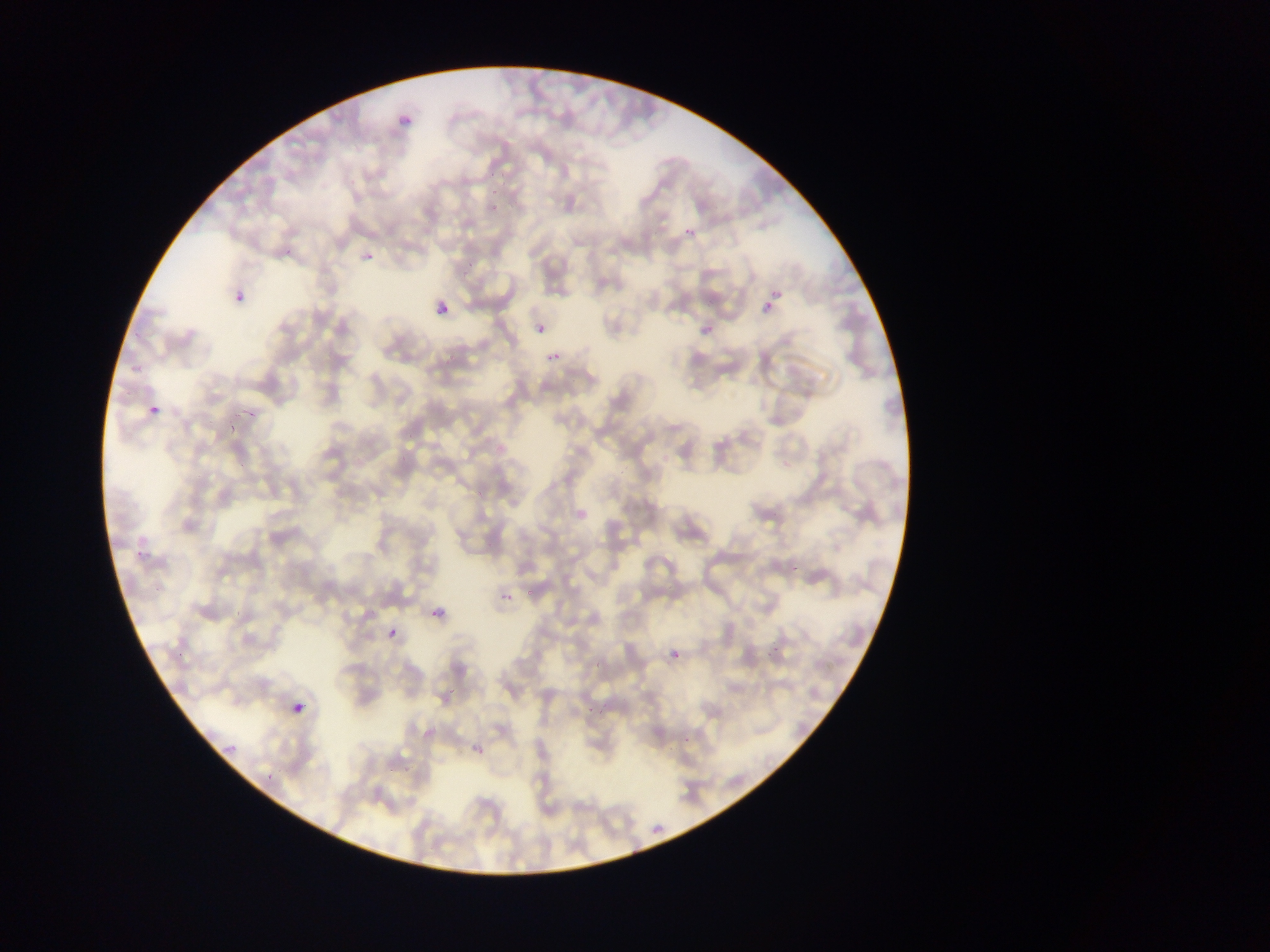

Approximate bounding boxes as {left, top, right, bottom} in pixels.
Summary:
  - Malaria parasite locations: {390, 107, 418, 128}, {481, 174, 515, 186}, {486, 195, 505, 214}, {684, 226, 694, 236}, {352, 246, 375, 268}, {772, 289, 784, 301}, {229, 290, 251, 304}, {427, 296, 457, 327}, {762, 303, 772, 314}, {695, 322, 723, 344}, {536, 325, 545, 335}, {541, 340, 571, 367}, {146, 403, 162, 416}, {236, 407, 262, 426}, {220, 426, 238, 445}, {134, 541, 148, 559}, {491, 588, 505, 605}, {427, 605, 440, 618}, {387, 627, 397, 637}, {671, 650, 680, 658}, {289, 688, 317, 714}, {212, 729, 253, 761}, {464, 738, 495, 765}, {646, 821, 664, 834}
  - Preparation: thin blood smear
  - Country: Ghana
  - Capture: mobile-phone photograph through a microscope
  - Image size: 1270×952 pixels
  - Field of view: single